Name the cell type shown.
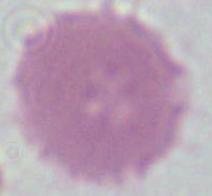
This is an erythrocyte.

Summary:
  - Modality: photomicrograph
  - Magnification: 1000x